State which parasite is depicted.
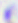
This is Toxoplasma gondii.

{
  "modality": "micrograph",
  "magnification": "400x"
}